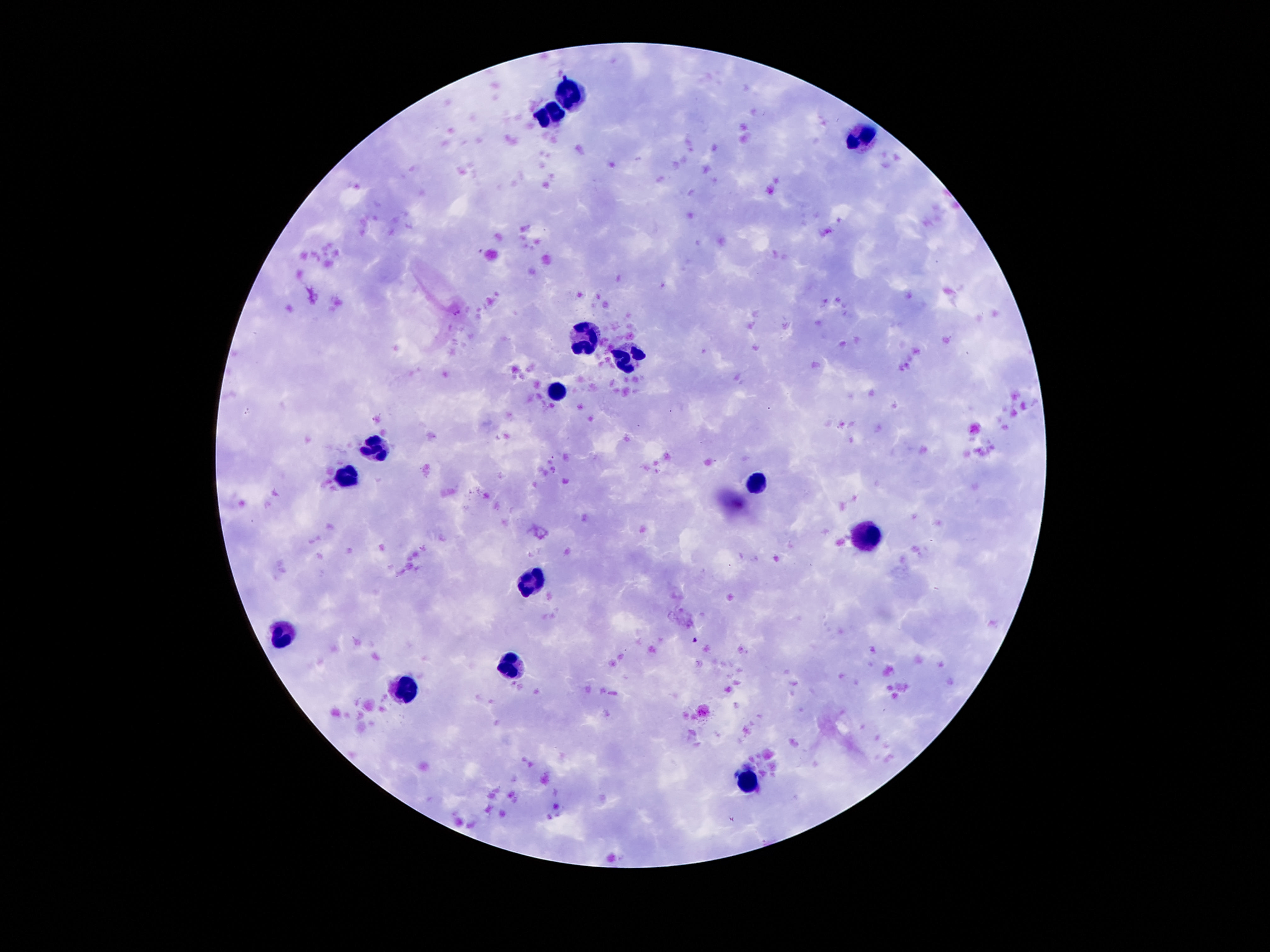
image size = 1270×952 pixels
stain = Giemsa
capture = smartphone camera through the microscope eyepiece
field of view = single
patient malaria status = not infected
preparation = thick blood film
leukocyte locations = approximate object centers, in pixels from the top-left corner: (x=571, y=92), (x=553, y=112), (x=860, y=137), (x=584, y=335), (x=627, y=356), (x=555, y=391), (x=375, y=446), (x=344, y=477), (x=754, y=483), (x=864, y=538), (x=530, y=585), (x=285, y=633), (x=510, y=667), (x=406, y=692), (x=746, y=782)
magnification = 100x